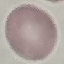
result: negative for malaria parasites
preparation: thin blood smear
stain: Giemsa
capture: smartphone through the microscope eyepiece
image_type: automatically extracted cell patch, resized to 64 × 64 pixels